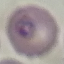
result = malaria parasites detected
preparation = thin blood film
stain = Giemsa
image type = cell patch, automatically extracted from a larger field of view and resized to 64 × 64 pixels
capture = smartphone through the microscope eyepiece